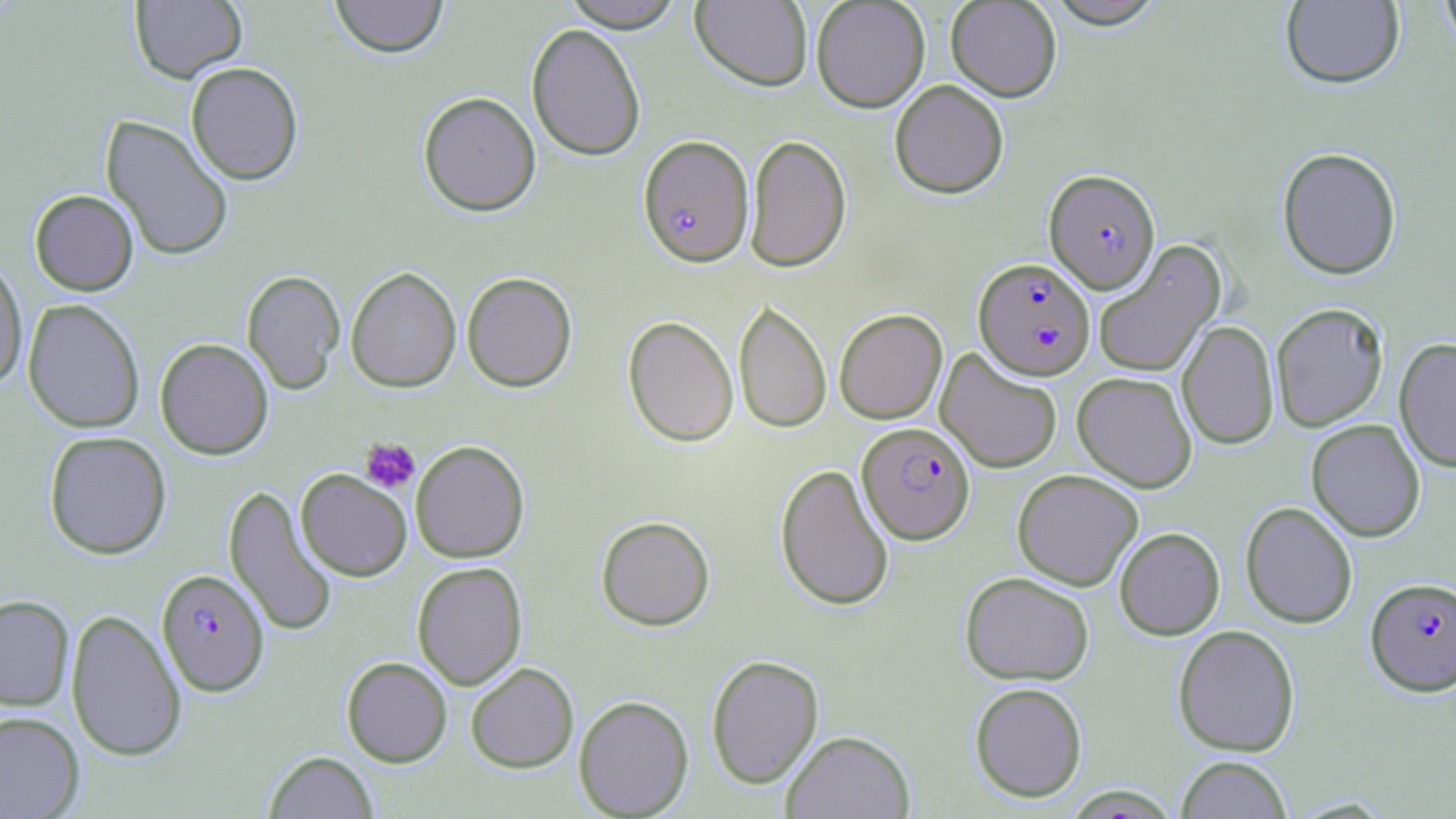

Summary:
  - Coordinate format: approximate bounding boxes as (x1,y1)-(x2,y2) corner pairs in pixels
  - Uninfected red blood cell locations: (130,0)-(246,83), (329,0)-(449,58), (561,0)-(685,31), (811,0)-(930,112), (946,0)-(1062,102), (1439,0)-(1456,59), (691,1)-(813,91), (1043,1)-(1169,29), (1280,1)-(1404,89), (526,23)-(646,161), (185,61)-(304,185), (889,79)-(1009,198), (418,91)-(541,216), (101,115)-(234,262), (745,134)-(852,272), (1277,147)-(1402,280), (29,189)-(139,295), (1093,239)-(1226,377), (0,257)-(28,391), (345,267)-(461,393), (242,270)-(345,394), (462,271)-(577,392), (23,299)-(145,433), (733,299)-(831,435), (1271,303)-(1389,432), (834,309)-(947,424), (623,315)-(738,447), (1178,320)-(1279,450), (155,338)-(274,459), (1394,338)-(1456,472), (935,347)-(1062,474), (1072,371)-(1198,492), (1307,419)-(1425,541), (44,430)-(171,559), (410,440)-(530,563), (775,463)-(895,612), (296,469)-(412,581), (1012,469)-(1142,591), (224,485)-(338,637), (1241,501)-(1357,628), (596,516)-(715,631), (1114,527)-(1225,640), (412,561)-(527,690), (960,571)-(1094,685), (0,595)-(74,710), (66,608)-(187,762), (1173,625)-(1300,757), (706,654)-(824,789), (341,657)-(452,767), (465,662)-(579,773), (969,681)-(1088,803), (573,695)-(694,818), (0,711)-(85,819), (781,730)-(915,819), (264,750)-(379,818), (1176,756)-(1293,819)
  - Plasmodium falciparum-infected red blood cell locations: (638,135)-(754,267), (1044,169)-(1160,294), (973,258)-(1096,380), (857,422)-(975,544), (156,569)-(269,696), (1366,577)-(1456,695)
  - Platelet locations: (360,437)-(420,493)
  - Slide-level diagnosis: Plasmodium falciparum
  - Modality: optical microscopy
  - Magnification: 1000x
  - Field of view: one of a larger specimen
  - Preparation: thin blood film
  - Stain: May-Grünwald-Giemsa
  - Image size: 1456×819 pixels